Report the malaria status of this cell.
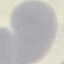
Uninfected.

Summary:
  - Preparation: thin blood film
  - Image type: automatically extracted cell patch, resized to 64 × 64 pixels
  - Stain: Giemsa
  - Capture: smartphone through the microscope eyepiece